Report the malaria status of this cell.
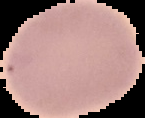
Uninfected.

image_type: segmented cell region with the area outside set to black
image_size: 145×118 pixels
preparation: thin blood smear